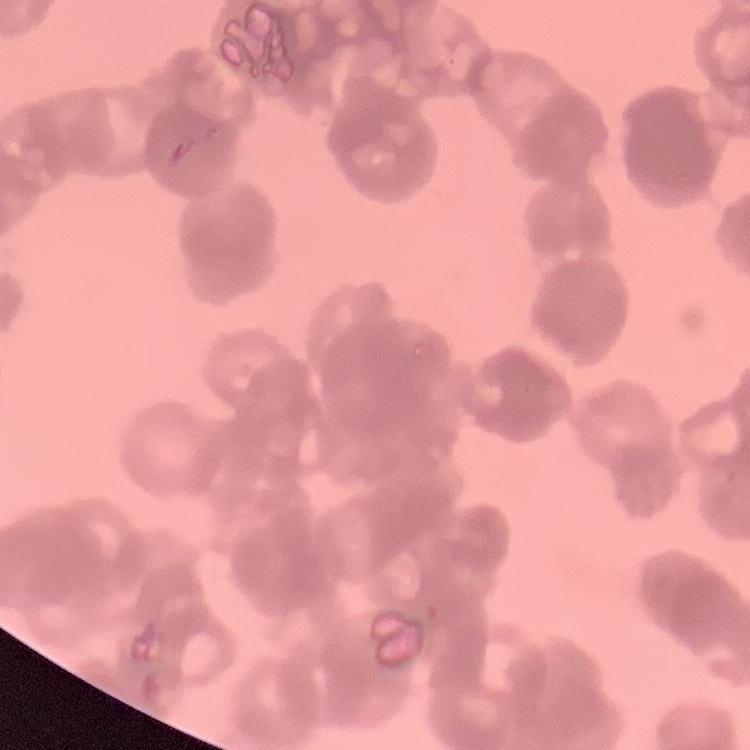

Summary:
  - Erythrocyte morphology: rouleaux formation
  - Stain: Field's or Giemsa
  - Preparation: thin blood film
  - Image type: one tile cut from a larger photomicrograph